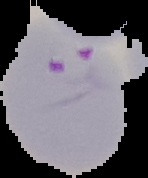

Summary:
  - Image size: 148×178 pixels
  - Image type: cell region segmented out of the field of view; surrounding area masked to black
  - Preparation: thin blood film
  - Result: malaria parasites detected